Give the extent of all Plasmodium falciparum-infected red blood cells.
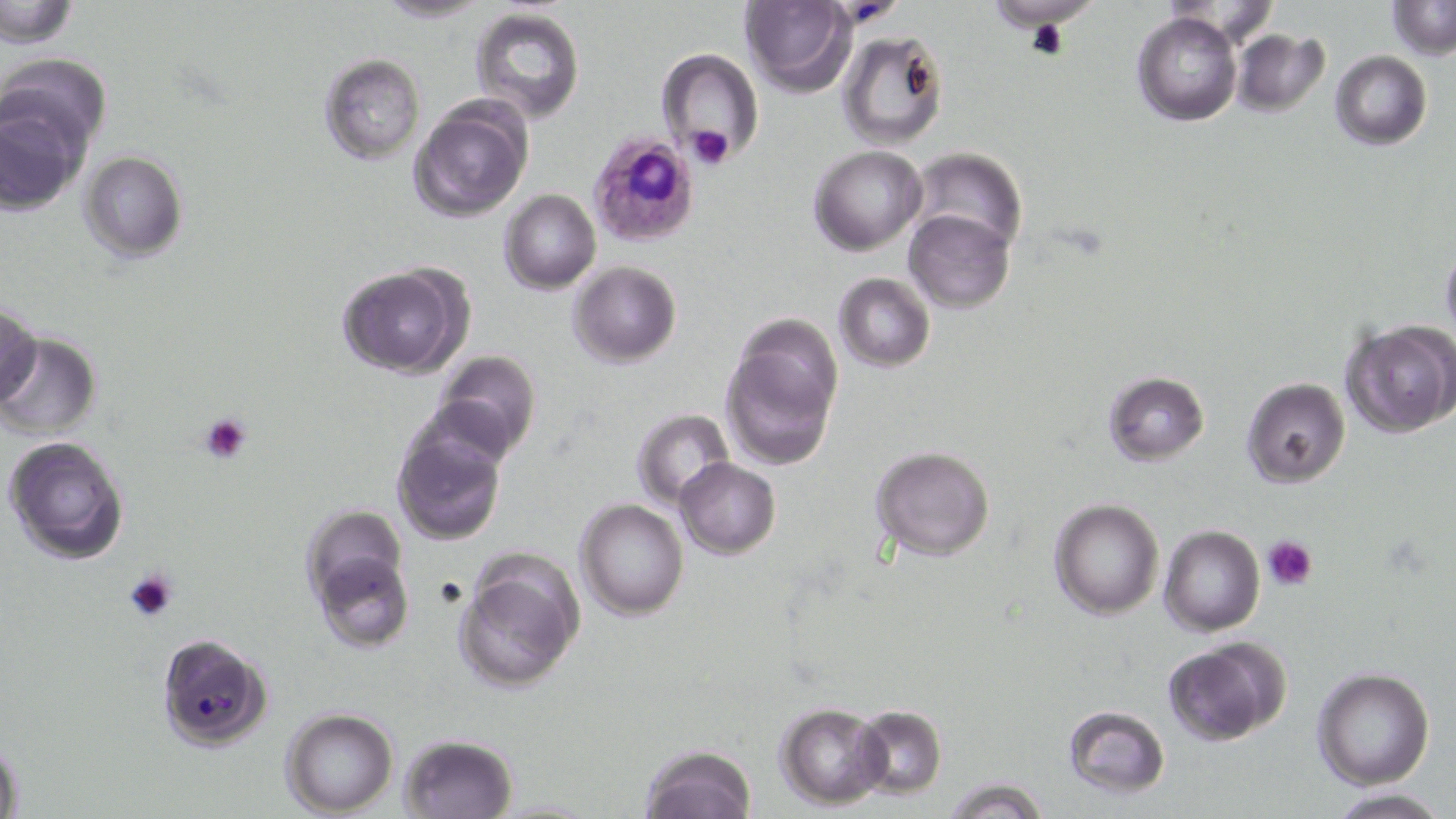

Approximate bounding boxes as [x1, y1, x2, y2] in pixels.
Plasmodium falciparum-infected red blood cells: [589, 131, 700, 248], [156, 633, 273, 750].

Summary:
  - Uninfected red blood cell locations: [371, 0, 493, 23], [1, 1, 80, 45], [739, 1, 854, 97], [1389, 1, 1454, 57], [984, 3, 1095, 35], [470, 6, 586, 124], [1132, 11, 1242, 126], [1231, 29, 1330, 117], [839, 31, 950, 151], [658, 50, 765, 165], [1330, 50, 1432, 150], [5, 53, 111, 158], [319, 54, 426, 164], [0, 97, 86, 213], [411, 99, 529, 221], [810, 144, 926, 255], [909, 148, 1026, 254], [79, 151, 188, 261], [501, 189, 600, 293], [905, 209, 1016, 313], [1439, 242, 1456, 346], [569, 261, 680, 367], [336, 263, 469, 379], [833, 274, 935, 372], [0, 305, 41, 408], [1342, 318, 1456, 438], [723, 324, 842, 471], [0, 333, 102, 440], [432, 350, 541, 460], [1102, 370, 1210, 464], [1241, 376, 1351, 488], [630, 409, 733, 507], [391, 418, 508, 545], [4, 432, 130, 565], [870, 445, 996, 562], [675, 458, 781, 557], [1049, 498, 1165, 620], [575, 499, 689, 621], [301, 506, 409, 609], [1158, 526, 1265, 636], [312, 552, 412, 653], [454, 556, 583, 695], [1164, 640, 1289, 746], [1312, 669, 1436, 791], [775, 702, 891, 808], [1062, 705, 1171, 796], [852, 706, 947, 798], [280, 709, 398, 816], [398, 733, 518, 818], [1, 735, 25, 819], [637, 744, 758, 818], [942, 777, 1048, 819], [1326, 788, 1448, 818]
  - Platelet locations: [686, 124, 734, 170], [199, 412, 252, 465], [1261, 535, 1318, 591], [125, 568, 179, 624]
  - Slide-level diagnosis: Plasmodium falciparum
  - Modality: light microscopy
  - Field of view: one of a larger specimen
  - Image size: 1456×819 pixels
  - Stain: May-Grünwald-Giemsa
  - Magnification: 1000x
  - Preparation: thin blood smear